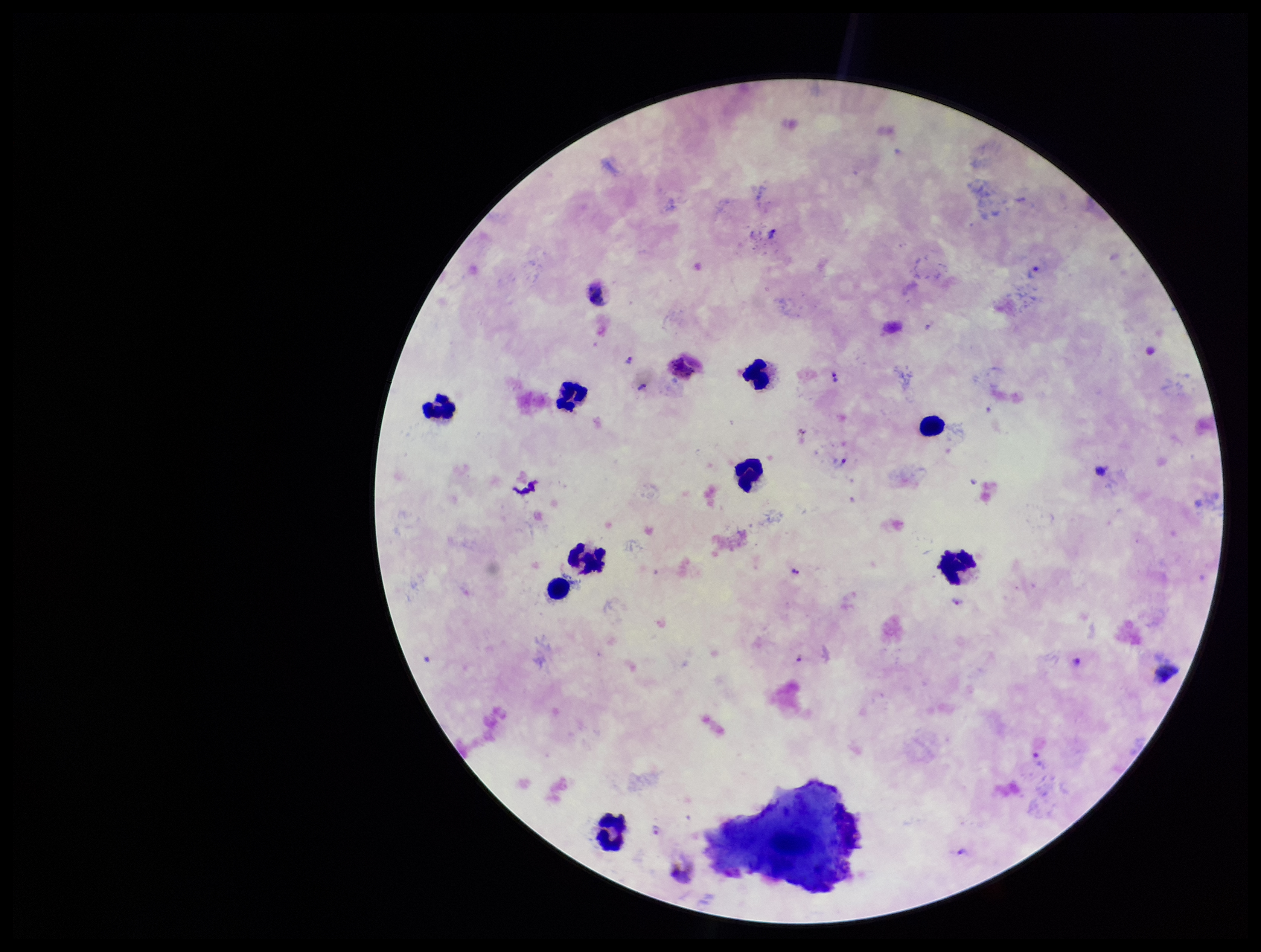
patient malaria status = positive
parasite count = 5
field of view = one from this slide
preparation = thick smear
species reported for this patient = Plasmodium vivax
leukocyte count = 9
capture = smartphone photograph through the microscope eyepiece
Plasmodium parasites = identified
image size = 1261×952 pixels
stain = Giemsa